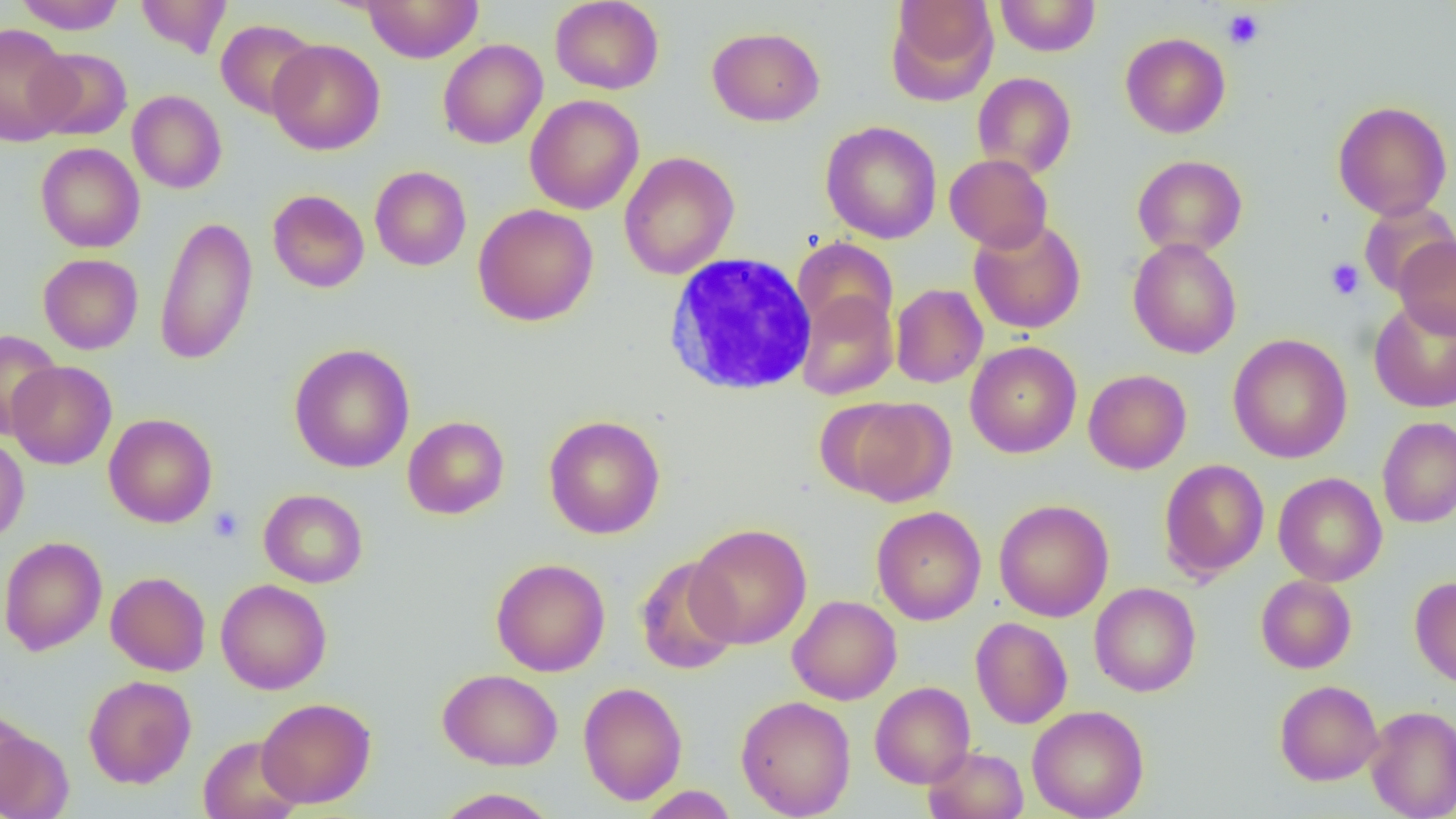 Approximate bounding boxes as (x1,y1)-(x2,y2) corner pairs in pixels. Platelet locations: (1223,8)-(1265,50), (1325,258)-(1365,300), (208,506)-(244,543). Uninfected red blood cell locations: (12,0)-(128,34), (135,0)-(232,57), (550,0)-(664,94), (885,0)-(998,104), (995,0)-(1101,56), (362,1)-(484,63), (216,19)-(320,120), (0,22)-(76,146), (707,26)-(824,126), (1120,32)-(1231,138), (267,38)-(385,155), (438,39)-(548,149), (29,48)-(132,140), (972,72)-(1077,179), (127,90)-(227,194), (525,95)-(644,215), (1332,100)-(1453,221), (821,121)-(942,244), (35,142)-(145,253), (619,151)-(739,280), (945,154)-(1052,253), (1133,154)-(1247,257), (370,166)-(471,271), (268,189)-(369,292), (1358,201)-(1456,297), (473,203)-(598,326), (154,215)-(258,365), (969,218)-(1086,334), (1394,236)-(1456,338), (792,237)-(899,339), (1128,238)-(1242,359), (38,254)-(143,354), (891,283)-(988,388), (796,290)-(898,400), (1369,298)-(1456,413), (0,329)-(62,438), (1228,333)-(1353,463), (965,341)-(1082,458), (289,343)-(415,473), (6,361)-(116,469), (1083,369)-(1192,474), (831,396)-(956,506), (104,413)-(217,528), (543,415)-(666,539), (402,416)-(509,519), (1377,416)-(1456,528), (0,436)-(29,543), (1158,459)-(1269,580), (1273,472)-(1387,586), (259,489)-(368,588), (994,499)-(1114,622), (871,505)-(986,625), (686,523)-(812,649), (0,536)-(107,656), (634,555)-(741,675), (490,558)-(610,676), (106,571)-(211,676), (1256,575)-(1356,673), (1410,576)-(1456,689), (216,578)-(332,695), (1089,582)-(1201,697), (788,595)-(902,705), (970,617)-(1073,729), (438,668)-(563,770), (83,675)-(196,788), (1274,679)-(1383,785), (870,681)-(975,788), (578,682)-(687,805), (736,695)-(856,818), (257,697)-(376,808), (1027,704)-(1149,819), (1365,706)-(1456,819), (0,711)-(45,815), (198,735)-(303,819), (924,746)-(1028,819), (639,785)-(737,819), (433,788)-(560,818). White blood cell locations: (663,252)-(817,397). Slide-level diagnosis: no evidence of blood parasites. 1000x magnification. Single field of view. Thin blood smear. Image is 1456×819 pixels. Light microscopy.